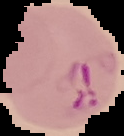

image type = cell region segmented out of the field of view; surrounding area masked to black
image size = 124×136 pixels
malaria status = parasitized
preparation = thin blood smear